Point out each leukocyte.
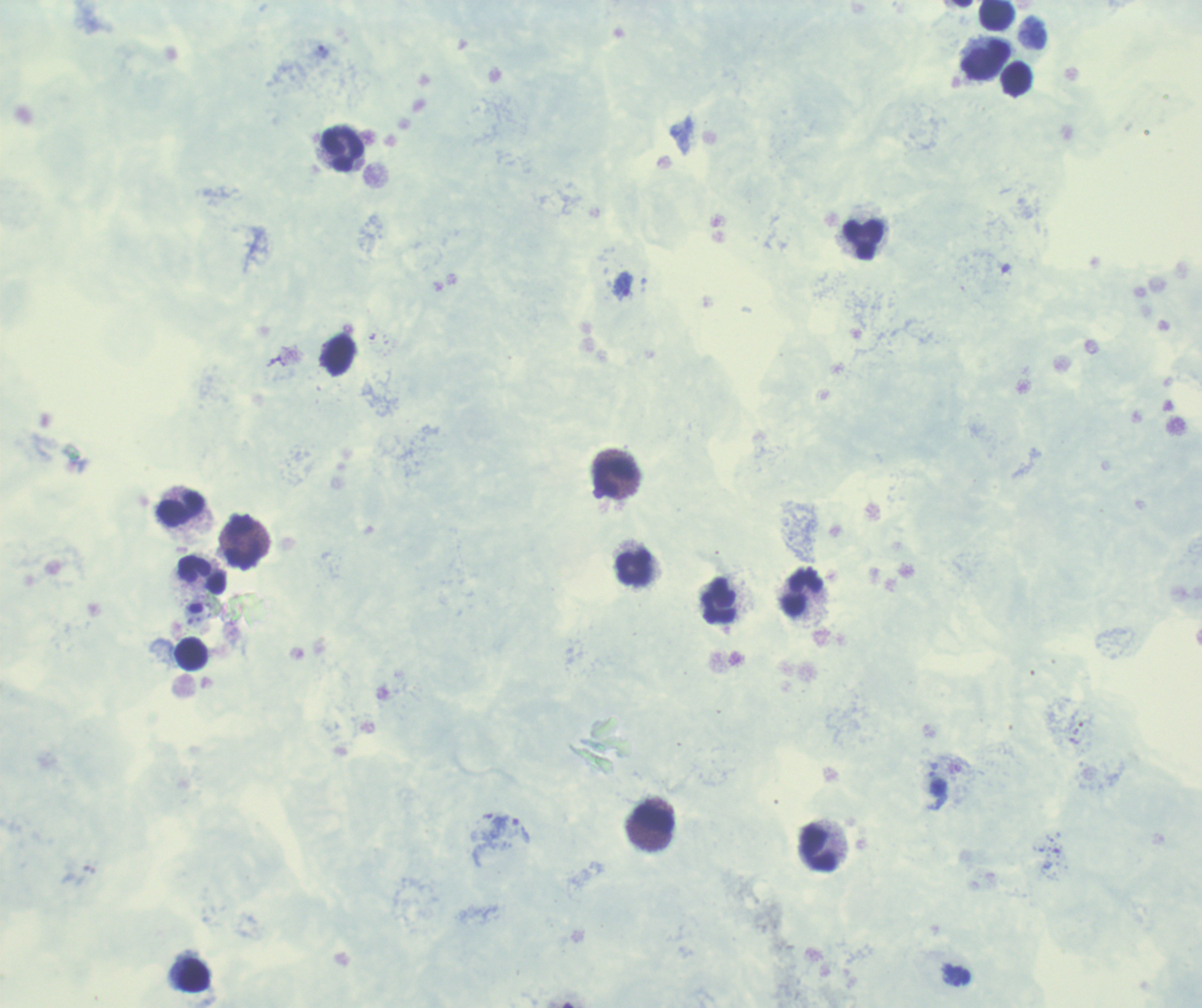

Approximate centers as [x, y] in pixels.
Leukocytes: [996, 14], [984, 60], [1017, 79], [344, 148], [864, 239], [615, 479], [182, 509], [243, 542], [635, 568], [201, 575], [803, 594], [720, 602], [192, 653], [654, 820], [820, 849], [194, 975].

Approximate centers as [x, y] in pixels.
Summary:
  - Trophozoite locations: [624, 284], [521, 830], [956, 975]
  - Preparation: thick blood film
  - Image size: 1202×1008 pixels
  - Context: previously used in an actual diagnosis
  - Result: positive for Plasmodium parasites
  - Stain: Romanowsky
  - Background quality: unsatisfactory
  - Field of view: single
  - Magnification: 100x